Locate and identify every blood parasite.
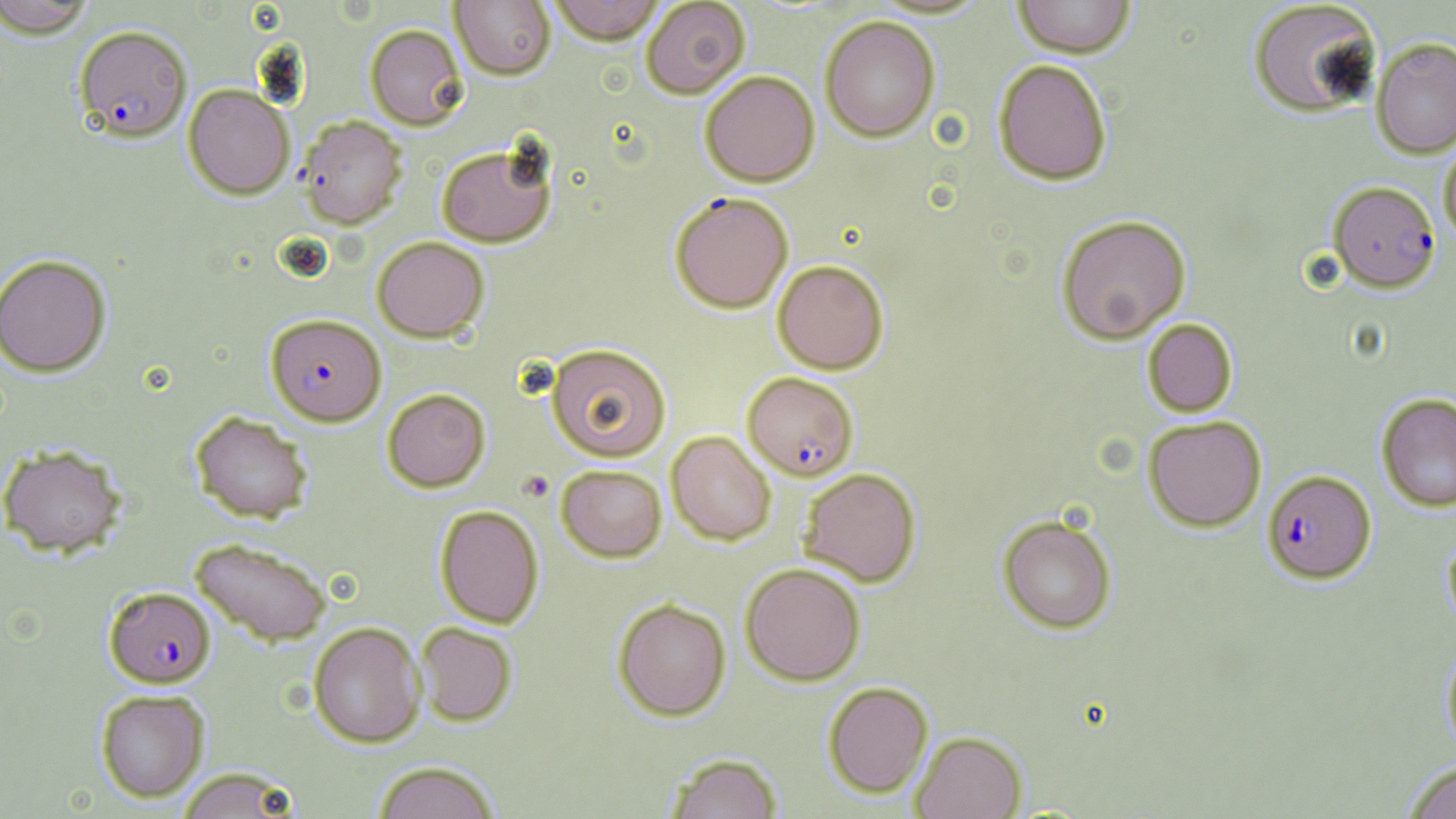

Approximate bounding boxes as (x1, y1, x2, y2) in pixels.
Plasmodium falciparum-infected red blood cells: (74, 24, 192, 142), (1328, 181, 1440, 292), (670, 191, 793, 313), (266, 313, 386, 425), (742, 372, 859, 481), (1262, 469, 1376, 584), (104, 586, 216, 688).
No Plasmodium ovale, Plasmodium malariae, Plasmodium vivax, Babesia divergens, or Trypanosoma brucei observed.

slide-level diagnosis = Plasmodium falciparum
magnification = 1000x
field of view = one of a larger specimen
preparation = thin blood smear
stain = May-Grünwald-Giemsa
modality = optical microscopy
image size = 1456×819 pixels
uninfected red blood cell locations = approximate bounding boxes as (x1, y1, x2, y2) in pixels: (1, 0, 97, 37), (450, 0, 556, 80), (546, 0, 665, 45), (640, 0, 750, 99), (1012, 0, 1136, 58), (1248, 1, 1383, 118), (820, 16, 940, 142), (365, 24, 468, 130), (1371, 37, 1456, 157), (993, 59, 1112, 185), (700, 71, 820, 186), (183, 84, 295, 199), (298, 115, 407, 229), (1438, 136, 1456, 244), (436, 143, 556, 247), (1056, 214, 1192, 344), (372, 236, 489, 342), (0, 253, 112, 376), (772, 259, 889, 374), (1142, 318, 1238, 417), (546, 343, 672, 462), (382, 388, 491, 492), (1376, 393, 1456, 512), (190, 411, 313, 523), (1143, 415, 1267, 531), (666, 431, 776, 545), (0, 443, 126, 557), (556, 464, 667, 562), (798, 467, 922, 587), (434, 505, 544, 628), (997, 514, 1117, 635), (1443, 530, 1456, 632), (189, 537, 332, 646), (740, 562, 866, 686), (613, 598, 731, 720), (308, 621, 426, 747), (415, 622, 517, 726), (1441, 638, 1456, 761), (823, 681, 933, 798), (95, 689, 209, 801), (911, 730, 1026, 819), (665, 753, 784, 819), (1401, 760, 1456, 819), (371, 761, 501, 819), (174, 767, 302, 818)